Identify the parasite.
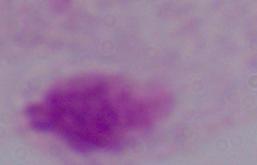

A trichomonad.

Captured at 1000x magnification. Micrograph.